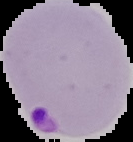

image size = 133×142 pixels
image type = segmented cell region with the area outside set to black
result = Plasmodium parasites detected
preparation = thin blood film